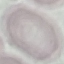
result: negative for malaria parasites
stain: Giemsa
preparation: thin blood film
capture: smartphone camera at the microscope eyepiece
image_type: automatically extracted cell patch, resized to 64 × 64 pixels